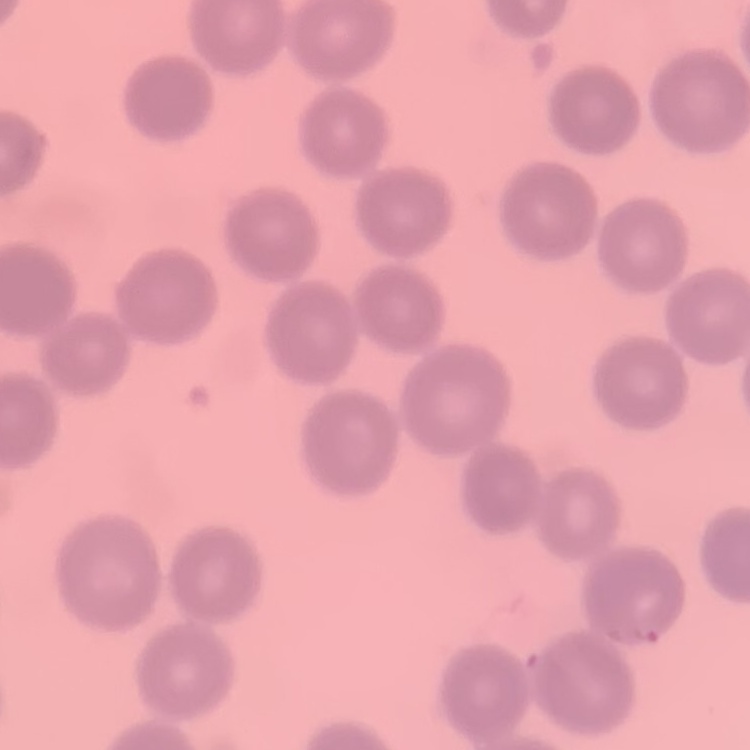

Summary:
  - Erythrocyte morphology: no rouleaux formation
  - Stain: Field's or Giemsa
  - Image type: one tile cut from a larger photomicrograph
  - Preparation: thin peripheral smear